Give the extent of all Plasmodium malariae-infected red blood cells.
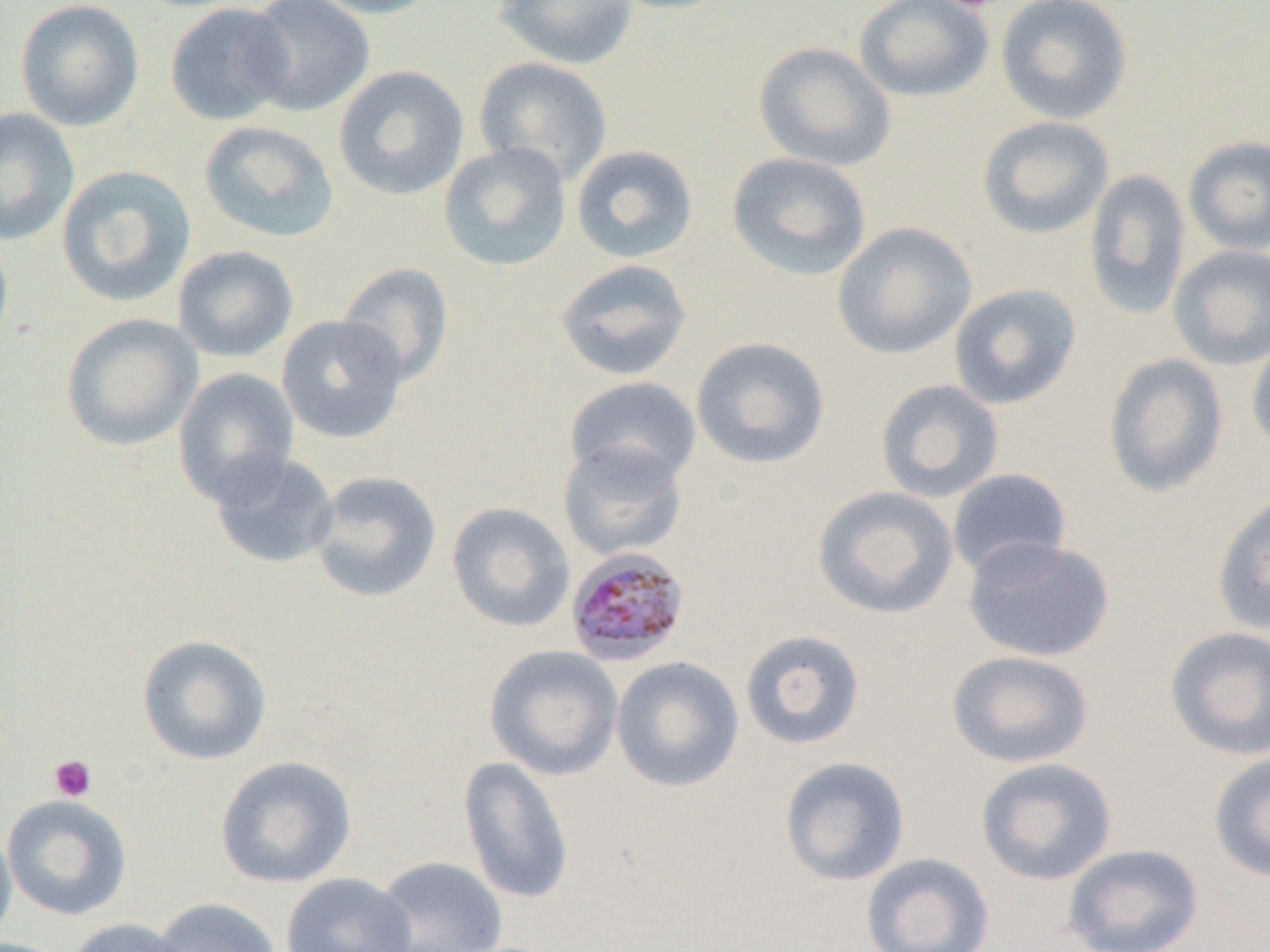

Approximate bounding boxes as (x1,y1)-(x2,y2) corner pairs in pixels.
Plasmodium malariae-infected red blood cells: (564,546)-(691,668).

slide-level diagnosis = Plasmodium malariae
modality = optical microscopy
magnification = 1000x
uninfected red blood cell locations = approximate bounding boxes as (x1,y1)-(x2,y2) corner pairs in pixels: (14,0)-(145,132), (243,0)-(375,117), (304,0)-(444,19), (493,0)-(640,70), (602,0)-(738,15), (854,0)-(994,102), (995,0)-(1134,125), (164,2)-(295,126), (753,41)-(896,172), (473,55)-(614,186), (333,65)-(470,201), (0,107)-(80,247), (977,115)-(1114,240), (199,120)-(340,243), (1183,135)-(1270,256), (438,142)-(572,272), (570,144)-(699,264), (726,151)-(872,282), (56,164)-(196,307), (1084,168)-(1191,320), (831,221)-(977,360), (0,231)-(14,360), (1167,244)-(1270,370), (172,245)-(298,363), (555,259)-(692,381), (336,262)-(454,389), (948,283)-(1082,410), (61,313)-(203,451), (276,314)-(407,444), (1247,331)-(1270,456), (690,336)-(831,470), (1102,353)-(1230,499), (172,367)-(300,507), (563,375)-(702,489), (874,378)-(1005,503), (557,440)-(689,562), (209,451)-(339,570), (947,469)-(1071,580), (308,470)-(442,603), (811,485)-(960,620), (1211,492)-(1270,635), (446,502)-(576,633), (962,535)-(1115,662), (1164,625)-(1270,761), (740,629)-(867,750), (136,634)-(272,766), (484,644)-(624,781), (946,650)-(1095,769), (610,656)-(745,793), (1208,751)-(1270,882), (215,755)-(357,888), (457,756)-(575,905), (779,756)-(911,886), (975,757)-(1118,886), (1,794)-(133,921), (0,819)-(17,946), (1062,843)-(1204,951), (861,852)-(995,952), (371,855)-(508,952), (281,872)-(417,952), (151,897)-(283,952), (66,918)-(192,952)
platelet locations = approximate bounding boxes as (x1,y1)-(x2,y2) corner pairs in pixels: (943,0)-(1003,12), (48,754)-(97,802)
field of view = one of a larger specimen
image size = 1270×952 pixels
preparation = thin blood smear